State which parasite is depicted.
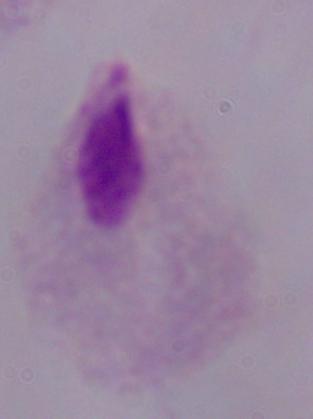

This is a trichomonad.

{
  "magnification": "1000x",
  "modality": "micrograph"
}